Point out each Plasmodium parasite and each leukocyte.
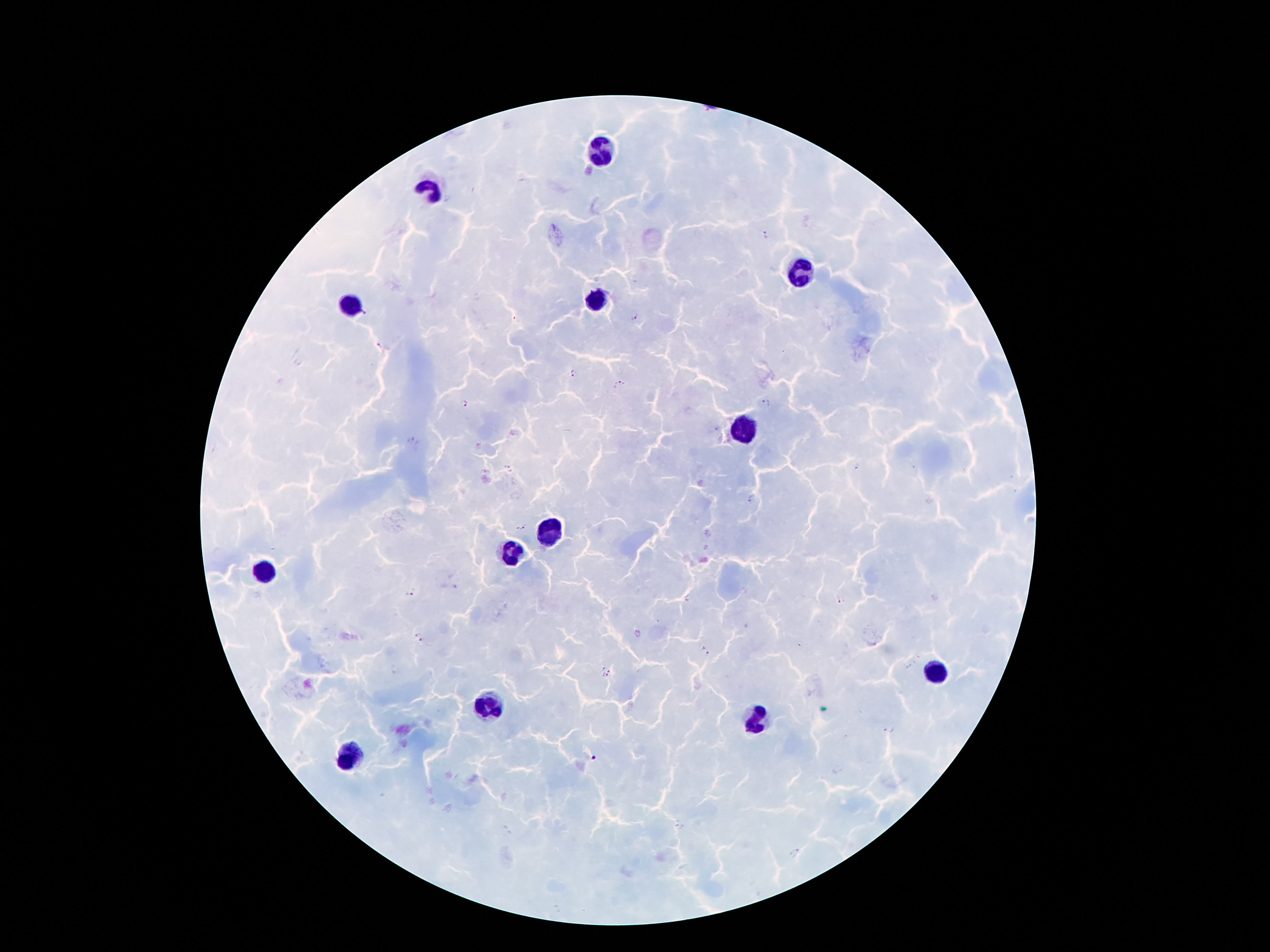
Approximate centers as [x, y] in pixels.
Plasmodium parasites: [764, 236], [366, 312], [635, 317], [380, 346], [573, 372], [620, 385], [766, 402], [464, 405], [412, 442], [856, 466], [509, 469], [753, 498], [522, 527], [412, 593], [840, 601], [419, 636], [705, 651], [909, 666], [607, 672], [889, 728], [593, 758], [679, 826], [795, 854].
Leukocytes: [600, 153], [433, 189], [801, 273], [595, 300], [351, 303], [746, 428], [554, 528], [511, 554], [265, 571], [936, 672], [490, 706], [757, 722], [356, 756].

Thick blood smear. 100x magnification. Photographed through the microscope eyepiece with a smartphone camera. Patient malaria status: positive for Plasmodium falciparum. Single field of view. Image is 1270×952 pixels. Giemsa stain.